Describe the morphology of the erythrocytes.
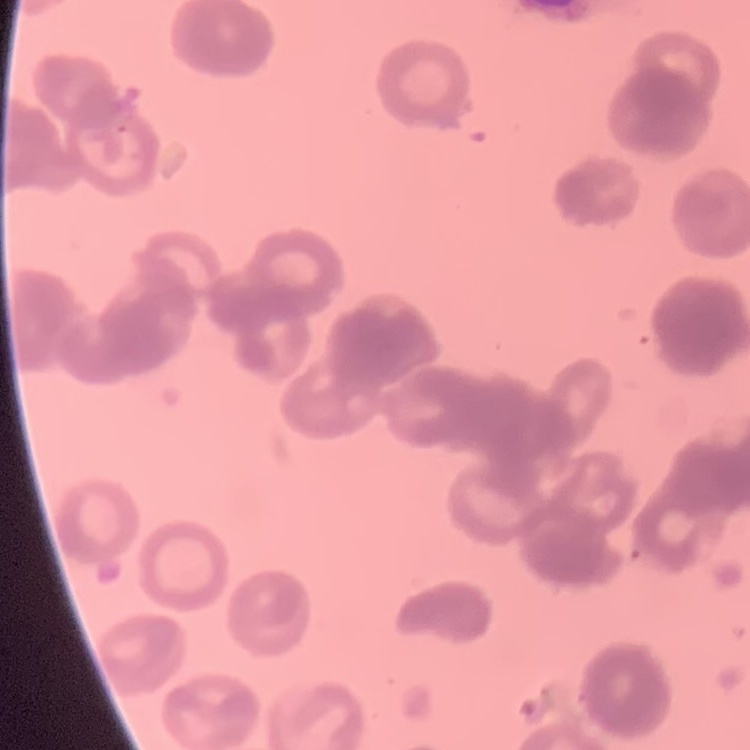
Rouleaux formation.

Summary:
  - Stain: Field's or Giemsa
  - Image type: one tile cut from a larger photomicrograph
  - Preparation: thin blood film